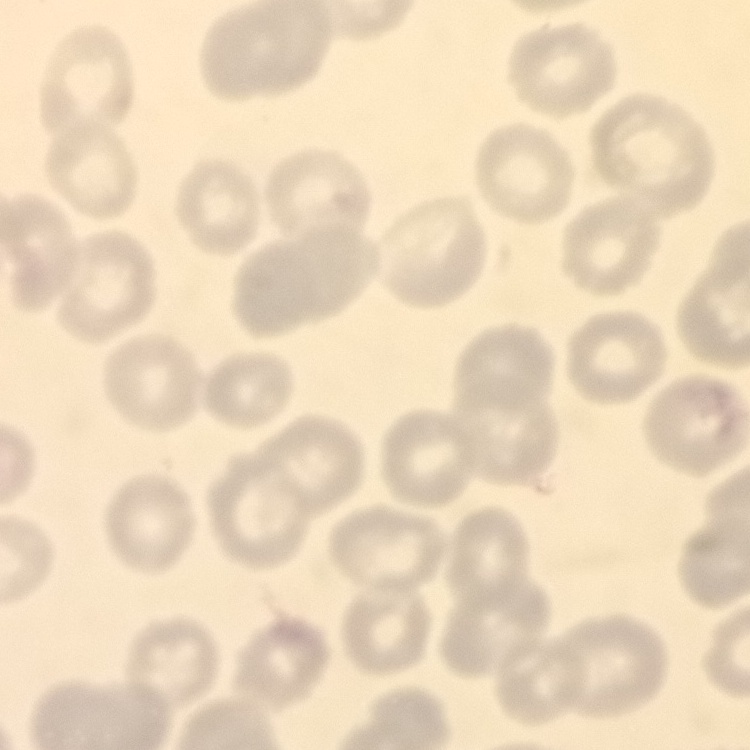 The red blood cells show no rouleaux formation. Stained with either Field's or Giemsa. One tile cut from a larger photomicrograph. Thin blood smear.